Mark where platelets are.
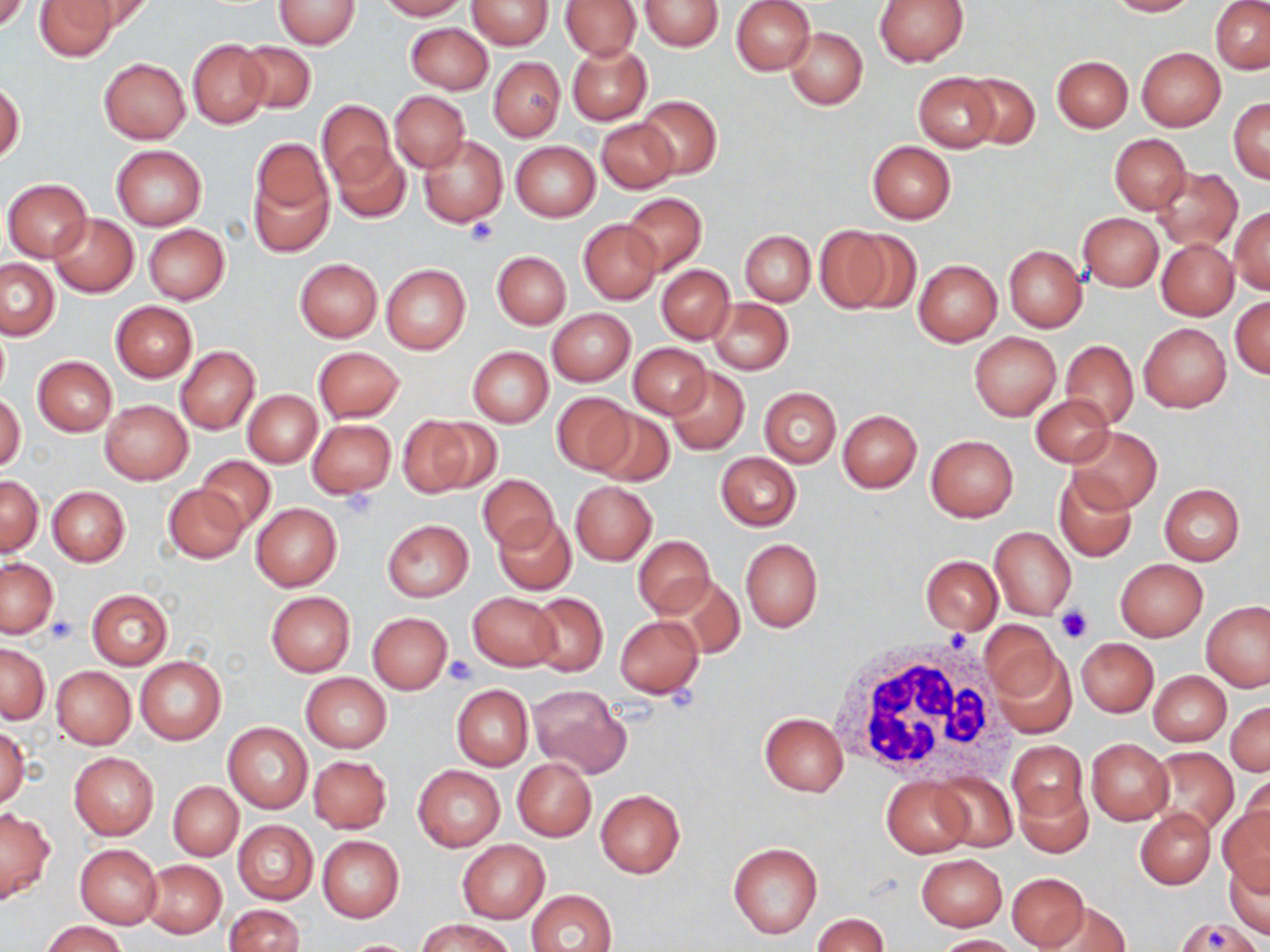
Approximate bounding boxes as [x1, y1, x2, y2] in pixels.
Platelets: [464, 217, 497, 247], [339, 488, 379, 522], [1057, 608, 1092, 644], [48, 618, 79, 645], [443, 654, 479, 686].

Uninfected red blood cell locations: [0, 0, 29, 34], [36, 0, 117, 60], [275, 0, 360, 49], [376, 0, 466, 20], [467, 0, 553, 49], [639, 0, 723, 51], [731, 0, 815, 75], [873, 0, 967, 67], [1104, 0, 1196, 16], [65, 1, 152, 42], [561, 1, 639, 60], [1211, 2, 1270, 73], [405, 22, 492, 93], [785, 27, 868, 110], [187, 39, 269, 129], [237, 41, 315, 113], [567, 43, 651, 124], [1136, 47, 1226, 130], [1052, 55, 1132, 132], [99, 57, 190, 143], [488, 57, 564, 141], [913, 73, 999, 153], [962, 73, 1039, 150], [0, 80, 25, 165], [389, 91, 470, 171], [635, 96, 722, 180], [1228, 98, 1270, 183], [317, 99, 393, 187], [596, 117, 677, 194], [419, 133, 508, 227], [1109, 134, 1191, 214], [250, 138, 330, 223], [866, 140, 956, 224], [510, 141, 600, 222], [332, 144, 410, 223], [111, 145, 206, 230], [1151, 167, 1241, 251], [250, 173, 332, 257], [3, 179, 93, 261], [623, 193, 707, 276], [1229, 207, 1270, 293], [1077, 213, 1163, 291], [51, 214, 138, 296], [579, 219, 661, 304], [143, 224, 230, 304], [815, 226, 892, 313], [740, 230, 814, 306], [843, 232, 920, 314], [1156, 238, 1238, 320], [1004, 246, 1086, 332], [492, 250, 570, 329], [295, 258, 382, 342], [913, 259, 1002, 346], [1, 260, 59, 340], [381, 264, 470, 355], [657, 265, 734, 344], [1230, 297, 1270, 378], [707, 298, 793, 375], [110, 301, 197, 381], [548, 308, 635, 386], [1139, 323, 1231, 412], [0, 325, 10, 402], [969, 332, 1061, 420], [1062, 340, 1138, 429], [628, 343, 711, 419], [175, 346, 261, 434], [314, 346, 403, 422], [467, 346, 553, 428], [33, 355, 118, 436], [667, 368, 748, 454], [759, 386, 840, 468], [244, 390, 321, 468], [0, 392, 25, 473], [1032, 392, 1116, 467], [550, 393, 636, 476], [101, 401, 192, 484], [590, 407, 673, 486], [837, 409, 921, 492], [398, 415, 486, 499], [307, 419, 395, 499], [1068, 427, 1161, 513], [925, 434, 1018, 521], [716, 451, 801, 531], [195, 455, 275, 534], [1053, 472, 1137, 562], [478, 473, 558, 552], [1, 475, 42, 556], [570, 481, 657, 565], [163, 483, 249, 564], [1159, 484, 1244, 565], [47, 486, 129, 566], [251, 503, 342, 591], [494, 513, 576, 595], [381, 519, 474, 602], [989, 526, 1075, 619], [633, 535, 714, 617], [740, 539, 823, 633], [922, 542, 1072, 626], [920, 554, 1002, 635], [2, 558, 57, 637], [1116, 559, 1207, 641], [657, 575, 743, 661], [86, 589, 173, 669], [266, 591, 355, 677], [467, 593, 559, 670], [527, 593, 607, 675], [1202, 600, 1270, 690], [368, 613, 452, 694], [614, 615, 705, 698], [980, 622, 1060, 707], [1076, 638, 1158, 716], [1, 644, 49, 724], [989, 646, 1077, 740], [135, 656, 225, 744], [51, 667, 136, 750], [1148, 670, 1231, 746], [301, 673, 391, 753], [451, 685, 534, 770], [527, 685, 631, 778], [1227, 700, 1269, 776], [520, 701, 613, 836], [759, 712, 848, 797], [223, 721, 313, 813], [0, 726, 29, 809], [1087, 738, 1172, 826], [1009, 741, 1087, 824], [1149, 747, 1239, 835], [69, 752, 158, 839], [308, 755, 392, 833], [513, 758, 596, 841], [413, 765, 505, 851], [931, 772, 1016, 852], [1238, 775, 1270, 854], [880, 777, 975, 857], [168, 781, 243, 860], [1017, 782, 1092, 858], [595, 789, 685, 879], [1218, 803, 1270, 894], [0, 807, 55, 906], [1136, 807, 1216, 888], [232, 819, 317, 906], [318, 835, 404, 921], [457, 839, 550, 923], [728, 841, 822, 938], [75, 844, 161, 928], [916, 853, 1007, 931], [1223, 857, 1270, 938], [142, 860, 226, 938], [1007, 872, 1091, 951], [527, 889, 616, 952], [1045, 902, 1130, 951], [223, 904, 305, 952], [814, 913, 889, 951], [420, 917, 515, 952], [42, 920, 126, 952], [934, 934, 1020, 952], [337, 938, 421, 951]. White blood cell locations: [831, 636, 1015, 786]. Slide-level diagnosis: no evidence of blood parasites. May-Grünwald-Giemsa stain. Captured at 1000x magnification. One field of a larger specimen. Thin blood smear. Image is 1270×952 pixels. Light microscopy.